Assess this cell for malaria.
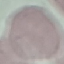
Uninfected.

Summary:
  - Stain: Giemsa
  - Preparation: thin blood smear
  - Image type: automatically extracted cell patch, resized to 64 × 64 pixels
  - Capture: smartphone camera at the microscope eyepiece